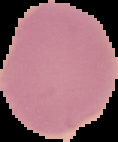

result: no Plasmodium parasites detected
image_size: 118×142 pixels
preparation: thin blood film
image_type: cell region segmented out of the field of view; surrounding area masked to black